Identify the parasite.
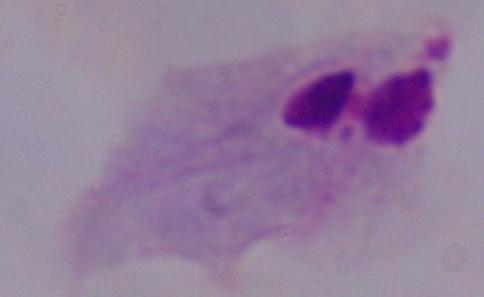

This is a trichomonad.

Summary:
  - Magnification: 1000x
  - Modality: micrograph